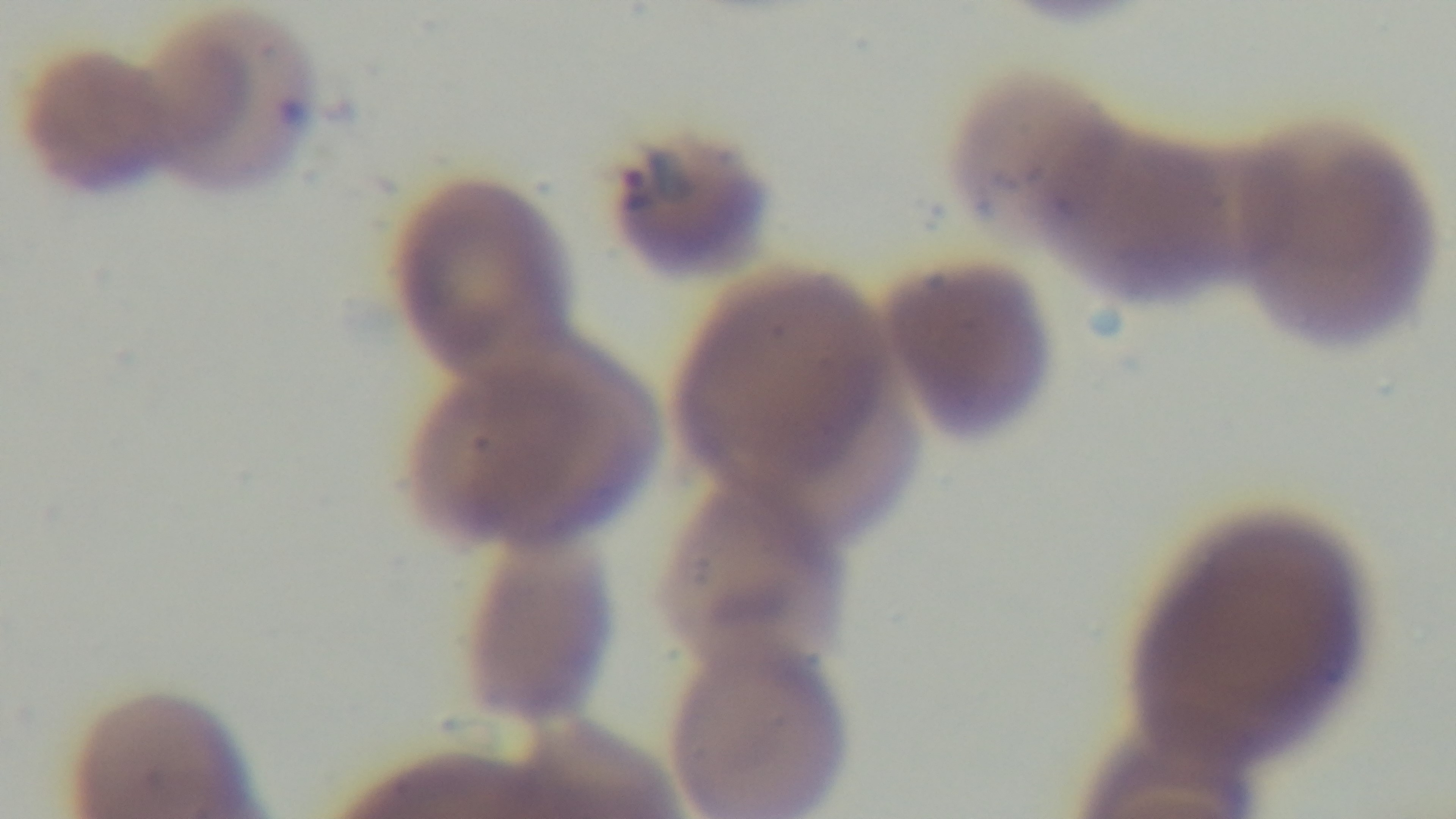
100x oil-immersion objective. Giemsa stain. Malaria status: positive. Captured with a mounted 4K digital camera. One field from the slide. Preparation: thin. Light microscopy.